Assess for Plasmodium parasites.
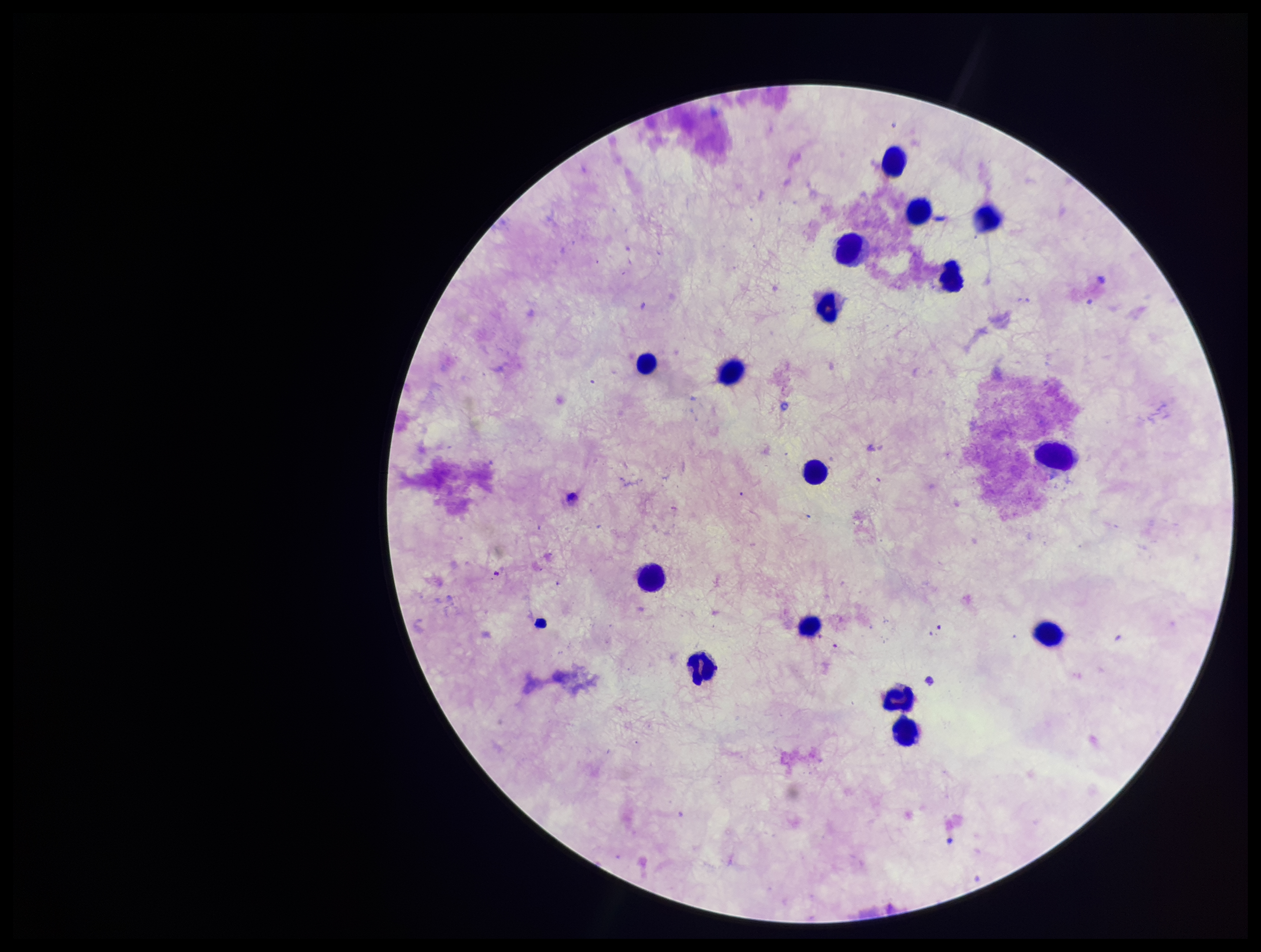

None identified.

{
  "preparation": "thick",
  "patient_malaria_status": "negative",
  "leukocyte_count": 16,
  "image_size": "1261×952 pixels",
  "field_of_view": "single",
  "stain": "Giemsa",
  "parasite_count": 0,
  "capture": "smartphone photograph through the microscope eyepiece"
}